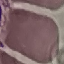 Result: no malaria parasites detected. Giemsa stain. Thin blood film. Automatically extracted cell patch, resized to 64 × 64 pixels. Acquired by smartphone through the microscope eyepiece.